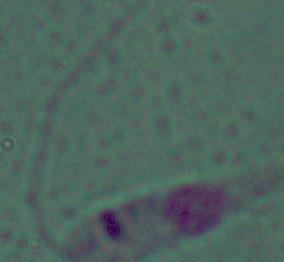
identification = Leishmania
modality = photomicrograph
magnification = 1000x